State the blood parasite species.
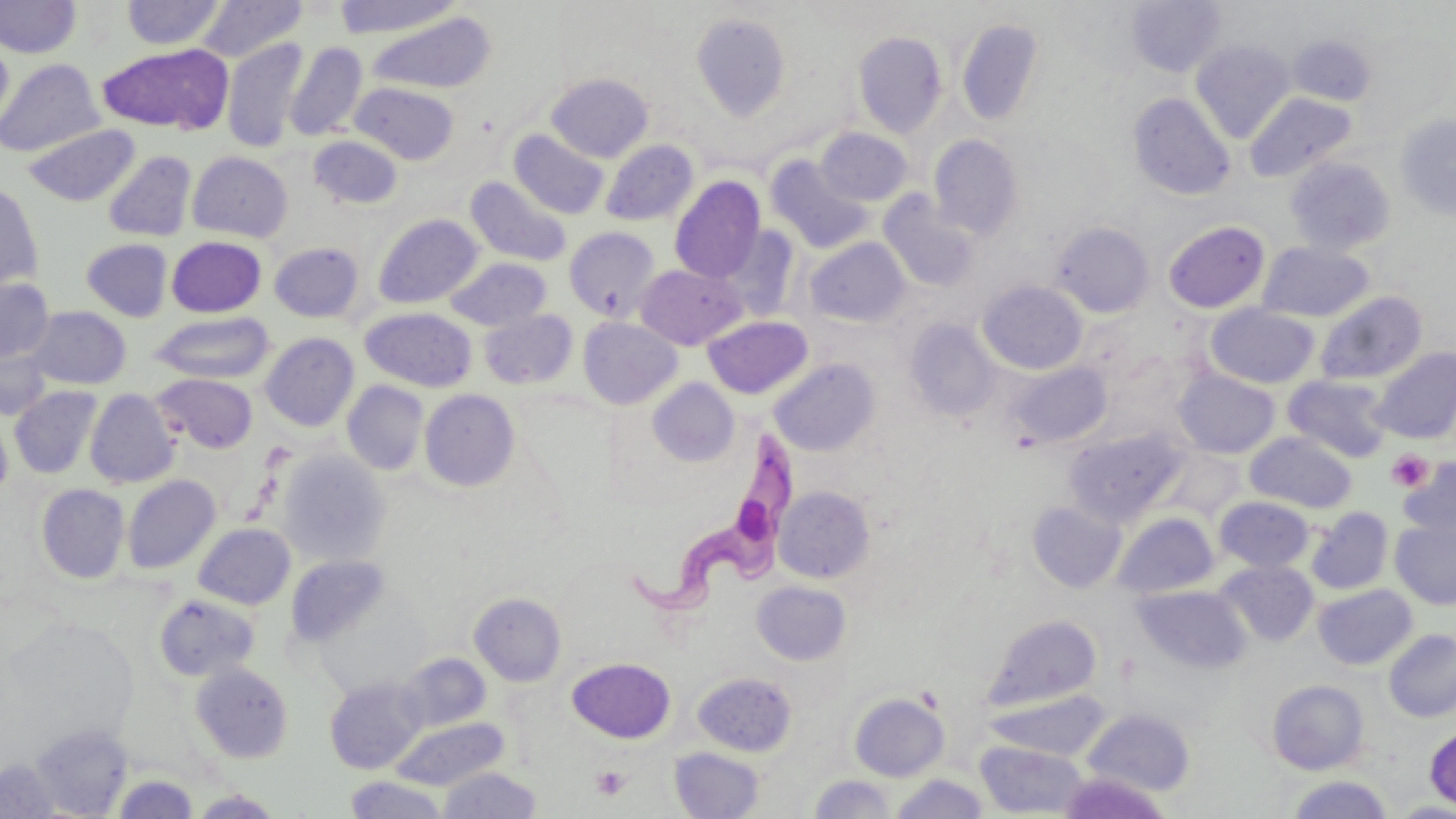

Trypanosoma brucei.

Approximate bounding boxes as (x1, y1, x2, y2) in pixels. Trypanosoma brucei locations: (630, 422, 795, 613). Platelet locations: (1386, 450, 1432, 492), (591, 766, 630, 801). Uninfected red blood cell locations: (332, 0, 463, 38), (1127, 0, 1226, 77), (0, 1, 80, 59), (121, 1, 226, 49), (195, 1, 308, 62), (365, 12, 497, 95), (691, 12, 792, 121), (956, 19, 1045, 126), (853, 30, 947, 138), (1288, 34, 1377, 106), (0, 36, 14, 138), (221, 37, 309, 152), (1191, 39, 1296, 142), (284, 42, 367, 142), (97, 43, 232, 134), (0, 59, 104, 157), (546, 73, 654, 162), (350, 81, 459, 165), (1128, 92, 1236, 200), (1246, 92, 1357, 182), (1394, 113, 1456, 222), (24, 125, 140, 206), (815, 128, 913, 206), (509, 129, 609, 219), (928, 134, 1024, 239), (308, 135, 404, 210), (600, 139, 698, 226), (103, 150, 197, 242), (187, 151, 292, 242), (766, 154, 875, 253), (1285, 157, 1396, 255), (466, 176, 573, 267), (669, 176, 766, 283), (0, 183, 43, 293), (879, 191, 980, 292), (372, 213, 484, 309), (1162, 220, 1270, 314), (1051, 221, 1154, 317), (564, 226, 662, 322), (167, 236, 266, 317), (804, 237, 911, 328), (81, 238, 172, 321), (270, 242, 364, 323), (1258, 242, 1374, 322), (445, 257, 551, 331), (635, 263, 748, 349), (0, 277, 55, 364), (978, 280, 1088, 375), (1315, 291, 1427, 386), (1206, 304, 1320, 388), (25, 306, 131, 390), (360, 307, 477, 392), (479, 309, 578, 390), (149, 312, 276, 383), (702, 315, 813, 399), (577, 316, 683, 409), (904, 319, 1001, 420), (261, 333, 359, 431), (0, 338, 52, 421), (1372, 347, 1456, 444), (769, 358, 881, 456), (1007, 361, 1111, 448), (1174, 369, 1280, 458), (153, 373, 258, 453), (1283, 375, 1392, 462), (647, 378, 740, 467), (342, 381, 430, 476), (9, 386, 102, 479), (85, 388, 181, 488), (419, 389, 520, 491), (0, 414, 12, 505), (1063, 426, 1189, 526), (1245, 431, 1357, 512), (277, 449, 391, 566), (1398, 457, 1456, 541), (122, 475, 220, 574), (36, 484, 130, 583), (774, 485, 875, 583), (1215, 496, 1314, 573), (1026, 500, 1126, 593), (1306, 507, 1394, 595), (1113, 513, 1219, 598), (1390, 519, 1456, 609), (193, 523, 296, 609), (285, 553, 390, 648), (1217, 560, 1319, 646), (752, 580, 851, 665), (1313, 583, 1418, 669), (1133, 584, 1251, 675), (469, 592, 566, 685), (154, 593, 261, 682), (985, 614, 1102, 711), (1384, 629, 1456, 722), (397, 653, 491, 732), (567, 657, 675, 743), (189, 661, 294, 763), (692, 671, 797, 756), (324, 676, 427, 774), (1266, 679, 1369, 775), (849, 692, 949, 781), (1082, 708, 1196, 797), (390, 717, 508, 790), (31, 723, 133, 817), (1425, 725, 1456, 811), (975, 740, 1089, 817), (669, 746, 765, 819), (0, 756, 61, 818), (438, 766, 543, 818), (891, 773, 989, 818), (110, 774, 199, 818), (808, 774, 898, 818), (1286, 774, 1394, 818), (345, 775, 448, 818), (190, 789, 284, 818). May-Grünwald-Giemsa stain. Thin blood smear. Image is 1456×819 pixels. Captured at 1000x magnification. Single field of view. Optical microscopy.